State which parasite is depicted.
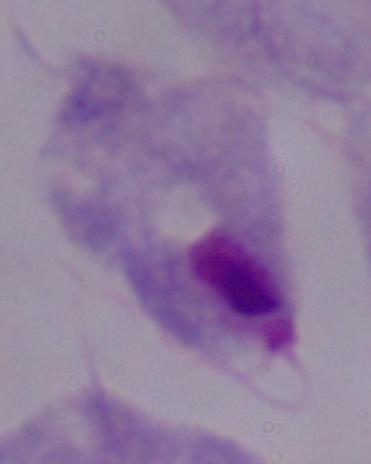
A trichomonad.

modality = photomicrograph
magnification = 1000x